Locate every blood parasite and identify its species.
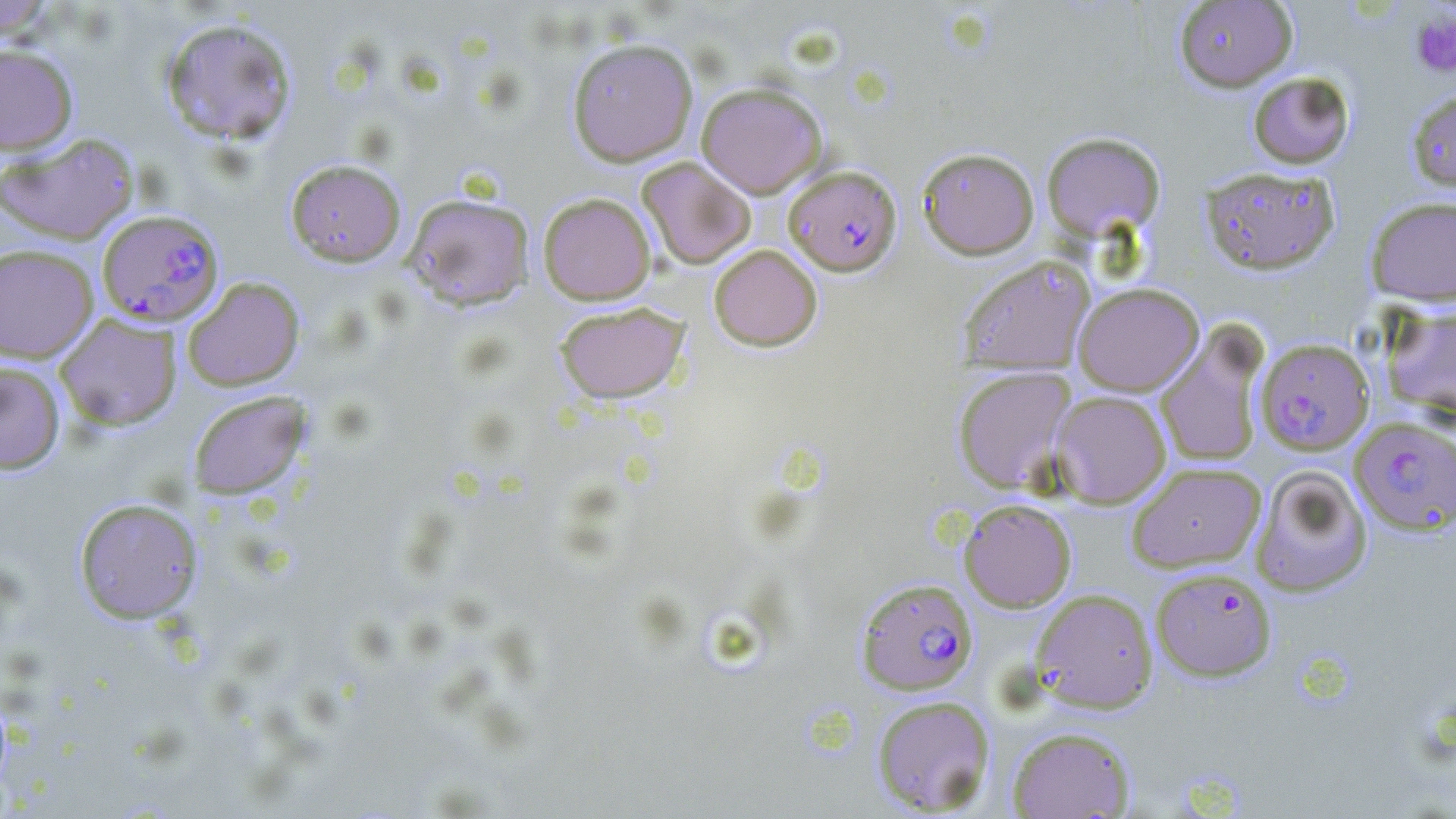
Approximate bounding boxes as [x1, y1, x2, y2] in pixels.
Plasmodium falciparum-infected red blood cells: [784, 165, 902, 275], [97, 209, 224, 327], [1255, 338, 1374, 454], [1350, 418, 1455, 535], [1151, 568, 1277, 682], [856, 577, 978, 695].
No Plasmodium ovale, Plasmodium malariae, Plasmodium vivax, Babesia divergens, or Trypanosoma brucei observed.

Platelet locations: [1410, 11, 1456, 79]. Uninfected red blood cell locations: [1174, 0, 1297, 92], [0, 1, 58, 39], [160, 17, 297, 145], [567, 38, 698, 166], [0, 42, 78, 154], [1247, 72, 1355, 169], [696, 82, 827, 198], [1406, 89, 1456, 195], [1041, 131, 1166, 241], [0, 132, 140, 245], [917, 147, 1039, 259], [637, 157, 756, 268], [285, 159, 406, 267], [1200, 166, 1340, 274], [403, 192, 534, 310], [538, 192, 656, 305], [1366, 196, 1456, 306], [0, 244, 99, 363], [708, 244, 823, 351], [958, 255, 1096, 375], [182, 277, 304, 391], [1073, 283, 1204, 396], [554, 302, 689, 404], [1379, 302, 1456, 422], [55, 314, 182, 430], [1155, 327, 1268, 468], [0, 362, 65, 474], [952, 366, 1076, 494], [188, 390, 310, 499], [1051, 391, 1171, 507], [1126, 461, 1267, 572], [1251, 464, 1373, 597], [73, 497, 203, 624], [958, 498, 1077, 612], [1031, 588, 1158, 713], [871, 695, 996, 815], [1006, 726, 1136, 818]. Slide-level diagnosis: Plasmodium falciparum. May-Grünwald-Giemsa-stained preparation. 1000x magnification. Thin blood smear. Light microscopy. Image is 1456×819 pixels. One field of a larger specimen.